Locate the red blood cells and classify each one as Plasmodium falciparum-infected, uninfected, or of indeterminate infection status.
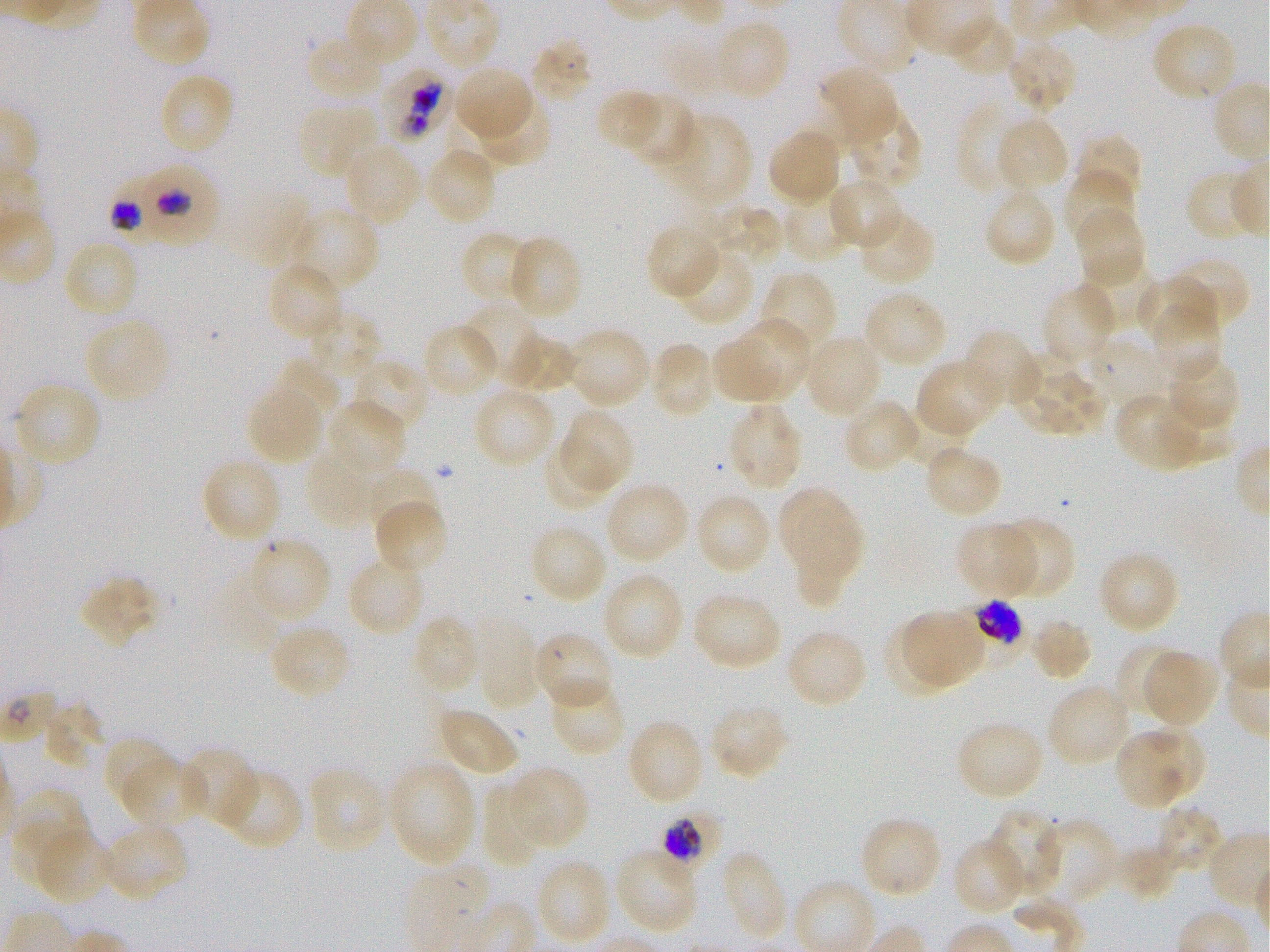

Approximate bounding boxes as (x1, y1, x2, y2) in pixels. Not every red blood cell is marked. A life-cycle stage — or a range of stages, where the recorded stages span more than one — follows each staged infected red blood cell.
Infected red blood cells: (383, 67, 449, 143) early trophozoite to early schizont; (143, 162, 220, 244) trophozoite; (112, 178, 173, 244) trophozoite; (971, 598, 1024, 647) late trophozoite to early schizont; (663, 814, 721, 868) trophozoite.
Uninfected red blood cells: (946, 17, 1017, 78), (714, 19, 792, 101), (1151, 21, 1237, 103), (530, 38, 595, 104), (1006, 39, 1078, 113), (308, 43, 383, 101), (817, 65, 899, 146), (454, 66, 533, 142), (164, 76, 232, 153), (595, 89, 662, 154), (627, 92, 698, 168), (477, 97, 552, 168), (956, 101, 1033, 195), (296, 104, 379, 181), (847, 108, 924, 192), (671, 113, 753, 206), (996, 116, 1069, 194), (767, 127, 841, 205), (1075, 133, 1143, 204), (347, 146, 422, 226), (430, 150, 495, 220), (1064, 168, 1135, 244), (1185, 168, 1260, 243), (828, 177, 904, 251), (983, 187, 1057, 268), (780, 193, 855, 264), (710, 203, 782, 264), (1074, 206, 1146, 288), (858, 211, 937, 286), (295, 212, 381, 295), (645, 224, 720, 300), (464, 234, 536, 306), (512, 238, 579, 318), (63, 239, 139, 319), (673, 248, 755, 328), (1168, 256, 1250, 332), (1080, 259, 1156, 331), (272, 268, 340, 335), (759, 270, 838, 356), (1136, 274, 1212, 343), (1041, 283, 1116, 367), (862, 291, 948, 370), (461, 302, 541, 382), (1149, 304, 1221, 382), (306, 309, 383, 383), (84, 318, 171, 404), (733, 319, 810, 398), (565, 326, 651, 408), (424, 327, 496, 392), (962, 328, 1041, 406), (503, 333, 578, 394), (803, 333, 882, 419), (1089, 335, 1168, 409), (708, 338, 782, 405), (649, 341, 716, 420), (1009, 351, 1078, 433), (1166, 354, 1242, 431), (274, 358, 341, 427), (360, 362, 426, 429), (918, 363, 999, 434), (1037, 370, 1105, 438), (20, 381, 100, 462), (247, 387, 323, 464), (471, 387, 557, 468), (1115, 391, 1206, 472), (1160, 395, 1234, 459), (331, 399, 407, 468), (842, 399, 921, 474), (727, 402, 805, 490), (895, 403, 966, 467), (561, 409, 635, 490), (543, 441, 617, 511), (923, 444, 1003, 520), (308, 452, 380, 527), (204, 462, 282, 539), (372, 467, 438, 536), (604, 482, 690, 563), (778, 486, 850, 564), (694, 492, 772, 575), (372, 499, 448, 575), (794, 513, 860, 605), (995, 516, 1075, 600), (955, 522, 1036, 598), (530, 524, 608, 604), (248, 537, 333, 621), (1098, 551, 1180, 634), (351, 554, 419, 629), (602, 571, 685, 660), (79, 573, 159, 649), (693, 592, 782, 671), (903, 610, 985, 683), (412, 614, 481, 694), (473, 616, 542, 710), (1028, 616, 1093, 682), (883, 622, 955, 696), (269, 623, 352, 700), (785, 628, 868, 710), (532, 630, 615, 711), (1115, 642, 1185, 719), (1143, 650, 1219, 727), (548, 678, 626, 757), (1047, 684, 1132, 767), (42, 701, 105, 769), (708, 703, 788, 780), (438, 708, 520, 778), (626, 718, 705, 807), (955, 720, 1045, 801), (1145, 724, 1204, 794), (1116, 727, 1186, 808), (104, 736, 176, 810), (180, 746, 258, 827), (124, 757, 209, 832), (388, 758, 480, 868), (307, 766, 389, 856), (507, 766, 589, 850), (217, 768, 304, 852), (481, 784, 543, 867), (15, 788, 90, 864), (1155, 808, 1221, 871), (986, 810, 1063, 894), (859, 817, 942, 901), (1040, 818, 1118, 905), (15, 820, 75, 881), (101, 823, 190, 902), (33, 827, 112, 905), (952, 837, 1027, 916), (1113, 845, 1177, 901), (614, 848, 699, 935), (718, 849, 789, 941), (538, 862, 609, 942).
No red blood cells of indeterminate infection status observed.

Summary:
  - Objective: 100x, oil immersion, numerical aperture 1.25
  - Field of view: single
  - Culture: static in-vitro Plasmodium falciparum strain 3D7
  - Preparation: thin blood smear
  - Stain: Giemsa
  - Donor blood group: O+
  - Image size: 1270×952 pixels